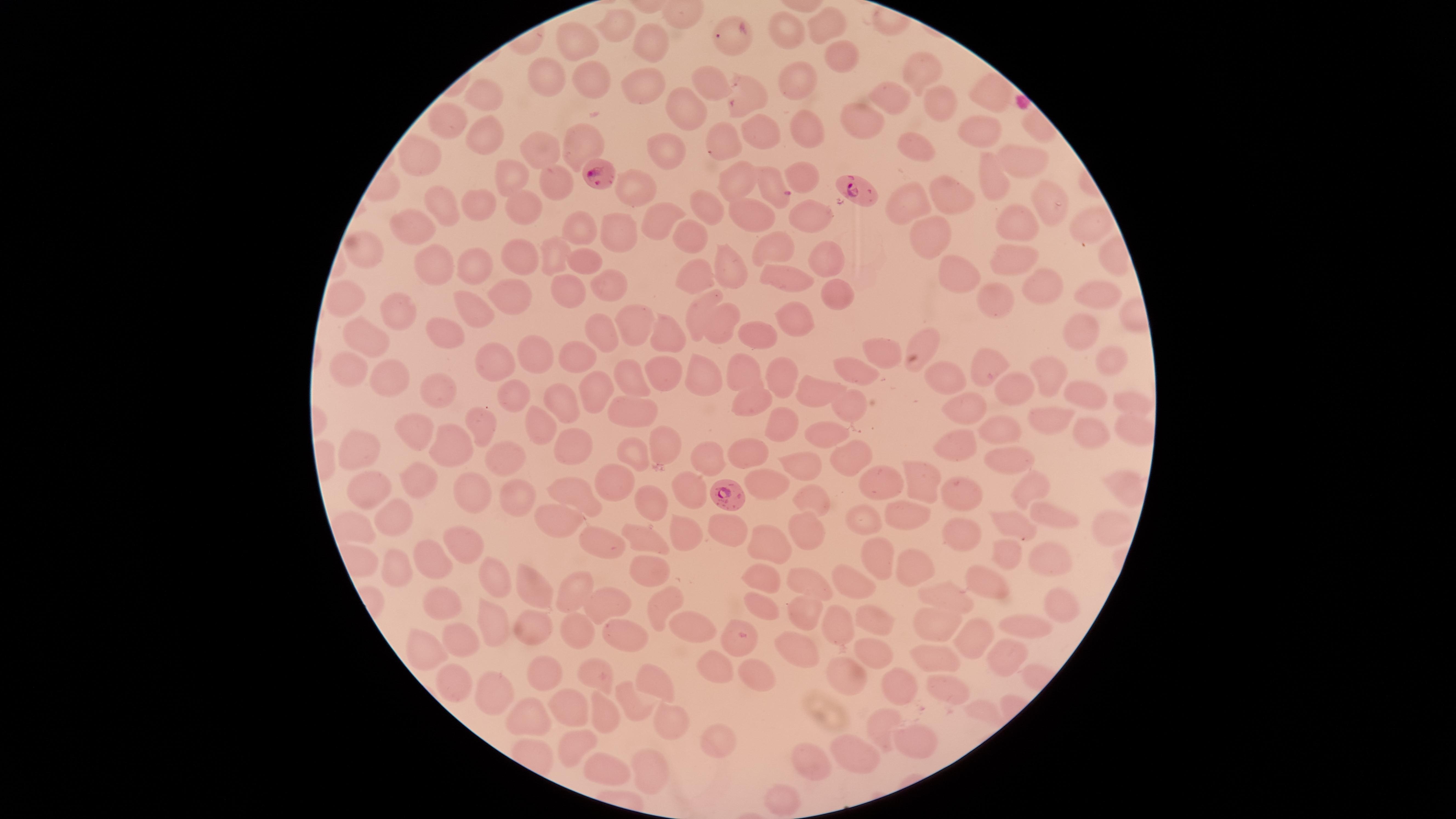

preparation: thin blood film
species: Plasmodium falciparum
field_of_view: single
parasitized_red_blood_cells: 'approximate marker points, in pixels from the top-left corner: (x=600, y=176), (x=775, y=189), (x=854, y=191), (x=730, y=494), (x=739, y=635)'
capture: smartphone photograph through the microscope eyepiece
uninfected_red_blood_cells: 'approximate marker points, in pixels from the top-left corner: (x=623, y=26), (x=825, y=27), (x=790, y=35), (x=729, y=36), (x=573, y=42), (x=653, y=47), (x=842, y=59), (x=911, y=70), (x=597, y=80), (x=709, y=81), (x=797, y=81), (x=645, y=82), (x=543, y=83), (x=988, y=93), (x=747, y=94), (x=893, y=97), (x=481, y=101), (x=935, y=102), (x=687, y=107), (x=859, y=119), (x=447, y=125), (x=808, y=128), (x=967, y=128), (x=756, y=133), (x=721, y=136), (x=491, y=139), (x=581, y=141), (x=667, y=144), (x=541, y=149), (x=915, y=149), (x=421, y=162), (x=1022, y=162), (x=741, y=174), (x=805, y=176), (x=508, y=183), (x=556, y=183), (x=988, y=184), (x=639, y=188), (x=1041, y=201), (x=949, y=202), (x=906, y=205), (x=478, y=206), (x=708, y=209), (x=521, y=211), (x=439, y=214), (x=810, y=215), (x=748, y=219), (x=653, y=221), (x=1091, y=221), (x=1014, y=222), (x=928, y=228), (x=415, y=230), (x=581, y=230), (x=685, y=235), (x=616, y=236), (x=770, y=251), (x=366, y=254), (x=556, y=256), (x=823, y=257), (x=1017, y=259), (x=584, y=260), (x=511, y=262), (x=428, y=263), (x=731, y=266), (x=474, y=267), (x=960, y=272), (x=787, y=277), (x=689, y=278), (x=1036, y=280), (x=610, y=286), (x=569, y=289), (x=833, y=291), (x=509, y=295), (x=993, y=295), (x=347, y=300), (x=1097, y=300), (x=478, y=313), (x=695, y=313), (x=398, y=316), (x=633, y=323), (x=793, y=326), (x=436, y=327), (x=722, y=327), (x=364, y=331), (x=749, y=334), (x=1074, y=334), (x=602, y=337), (x=665, y=341), (x=928, y=341), (x=883, y=350), (x=533, y=353), (x=573, y=356), (x=1109, y=356), (x=495, y=363), (x=987, y=363), (x=743, y=371), (x=346, y=372), (x=664, y=372), (x=862, y=372), (x=392, y=374), (x=777, y=374), (x=1047, y=374), (x=627, y=379), (x=947, y=380), (x=700, y=381), (x=595, y=386), (x=440, y=389), (x=1014, y=389), (x=508, y=391), (x=819, y=393), (x=1087, y=397), (x=853, y=399), (x=557, y=401), (x=1128, y=401), (x=963, y=405), (x=747, y=407), (x=638, y=408), (x=1052, y=418), (x=479, y=421), (x=543, y=425), (x=779, y=427), (x=417, y=428), (x=999, y=432), (x=822, y=437), (x=1086, y=437), (x=956, y=442), (x=663, y=443), (x=453, y=444), (x=571, y=446), (x=361, y=451), (x=511, y=454), (x=746, y=454), (x=635, y=456), (x=851, y=456), (x=707, y=458), (x=1002, y=460), (x=791, y=468), (x=416, y=479), (x=922, y=479), (x=616, y=481), (x=883, y=485), (x=763, y=486), (x=1025, y=486), (x=685, y=489), (x=572, y=492), (x=959, y=493), (x=368, y=496), (x=515, y=496), (x=812, y=499), (x=475, y=500), (x=644, y=508), (x=1034, y=514), (x=396, y=516), (x=862, y=518), (x=559, y=519), (x=906, y=519), (x=1018, y=524), (x=719, y=526), (x=1101, y=530), (x=958, y=534), (x=807, y=535), (x=683, y=537), (x=641, y=540), (x=464, y=541), (x=606, y=541), (x=765, y=543), (x=1006, y=555), (x=878, y=556), (x=1049, y=557), (x=436, y=559), (x=396, y=561), (x=643, y=563), (x=907, y=566), (x=804, y=576), (x=757, y=577), (x=491, y=579), (x=849, y=588), (x=992, y=588), (x=536, y=589), (x=570, y=594), (x=947, y=595), (x=611, y=604), (x=757, y=604), (x=660, y=606), (x=1060, y=606), (x=438, y=607), (x=804, y=609), (x=878, y=615), (x=493, y=621), (x=837, y=621), (x=934, y=623), (x=530, y=626), (x=689, y=626), (x=1022, y=626), (x=573, y=635), (x=625, y=639), (x=971, y=639), (x=460, y=645), (x=421, y=651), (x=803, y=656), (x=864, y=657), (x=930, y=657), (x=1000, y=657), (x=592, y=671), (x=755, y=671), (x=710, y=675), (x=541, y=678), (x=844, y=678), (x=654, y=680), (x=454, y=682), (x=945, y=686), (x=490, y=689), (x=900, y=691), (x=571, y=707), (x=631, y=707), (x=604, y=716), (x=880, y=718), (x=673, y=719), (x=526, y=723), (x=913, y=738), (x=569, y=739), (x=720, y=743), (x=855, y=757), (x=808, y=760), (x=655, y=772), (x=597, y=773), (x=783, y=797)'
image_size: 1456×819 pixels
visible_region: circular
presence: malaria parasites detected
stain: Giemsa